Locate and identify every blood parasite.
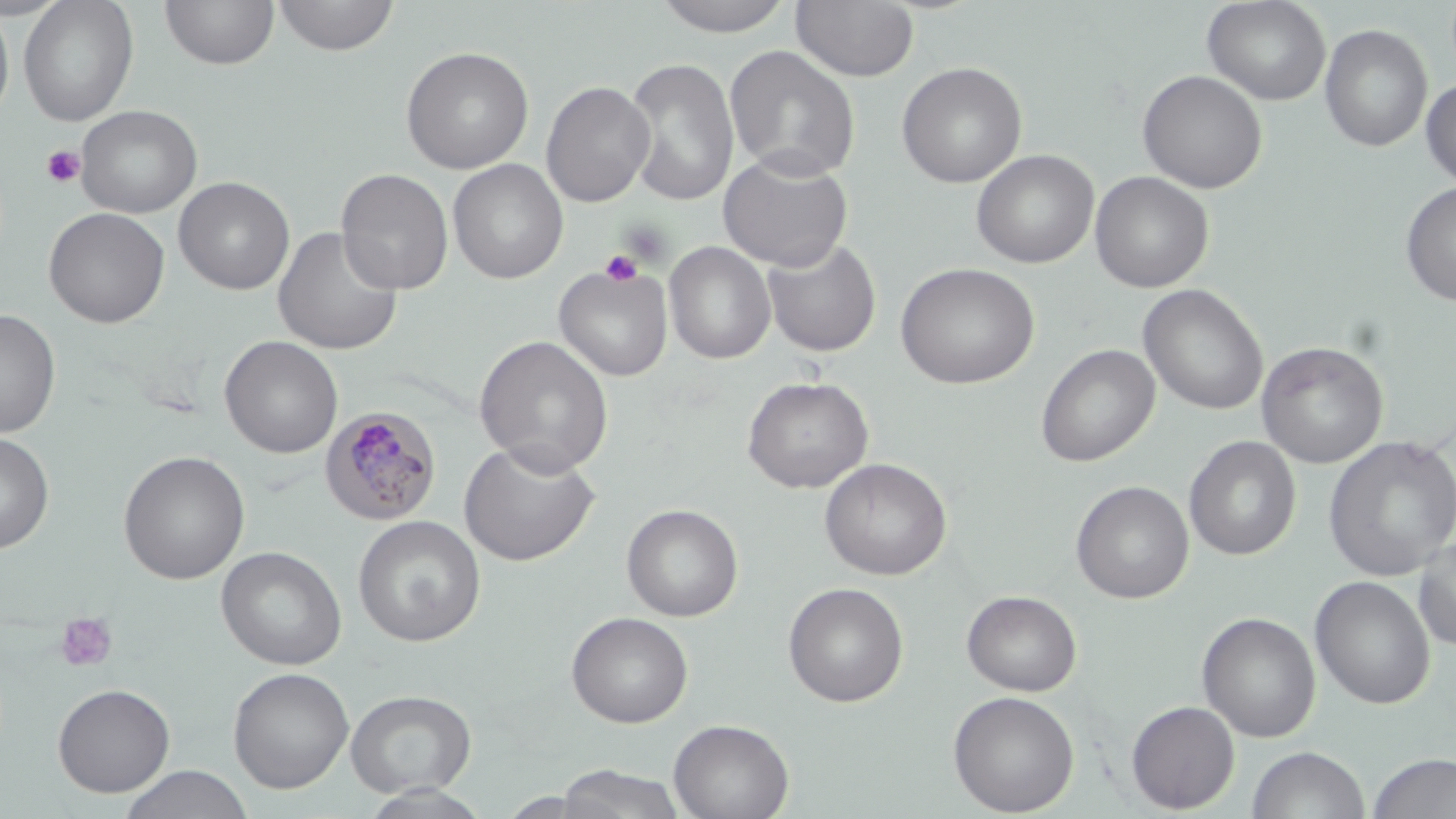

Approximate bounding boxes as (x1, y1, x2, y2) in pixels.
Plasmodium malariae-infected red blood cells: (321, 406, 441, 526).
No Plasmodium falciparum, Plasmodium ovale, Plasmodium vivax, Babesia divergens, or Trypanosoma brucei observed.

Uninfected red blood cell locations: (18, 0, 139, 126), (159, 0, 279, 71), (272, 0, 400, 57), (649, 0, 799, 37), (1202, 0, 1332, 106), (791, 1, 919, 83), (0, 4, 15, 126), (1319, 23, 1432, 153), (400, 45, 534, 174), (725, 45, 861, 182), (625, 57, 740, 207), (896, 61, 1027, 188), (1137, 69, 1268, 194), (1421, 77, 1455, 190), (541, 81, 654, 208), (76, 105, 202, 218), (971, 149, 1099, 269), (718, 150, 854, 271), (448, 159, 568, 284), (336, 168, 454, 295), (1089, 171, 1214, 293), (173, 176, 294, 295), (1400, 181, 1456, 307), (43, 207, 169, 328), (273, 225, 404, 355), (762, 237, 882, 358), (664, 241, 777, 364), (895, 262, 1040, 389), (553, 263, 673, 381), (1138, 284, 1269, 415), (0, 310, 61, 438), (219, 335, 343, 458), (474, 335, 614, 476), (1256, 340, 1388, 468), (1035, 344, 1160, 467), (741, 376, 874, 493), (0, 431, 55, 554), (1322, 434, 1456, 580), (1184, 436, 1301, 561), (459, 440, 601, 567), (118, 450, 250, 584), (819, 457, 952, 580), (1071, 480, 1194, 604), (622, 503, 744, 621), (353, 515, 485, 647), (1412, 535, 1456, 651), (216, 545, 347, 671), (1309, 575, 1435, 710), (783, 582, 909, 707), (961, 589, 1082, 696), (566, 611, 693, 728), (1196, 611, 1321, 742), (228, 667, 354, 794), (52, 683, 175, 797), (345, 689, 477, 797), (947, 689, 1080, 816), (1126, 700, 1240, 813), (669, 718, 794, 819), (1247, 746, 1370, 819), (1365, 752, 1456, 819), (553, 764, 687, 819), (118, 765, 255, 819), (356, 784, 495, 818), (498, 791, 603, 818). Platelet locations: (40, 145, 86, 187), (599, 249, 643, 287), (55, 612, 118, 672). Slide-level diagnosis: Plasmodium malariae. Image is 1456×819 pixels. Thin blood smear. One field of a larger specimen. Optical microscopy. Captured at 1000x magnification. May-Grünwald-Giemsa stain.